State which parasite is depicted.
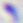
This is Toxoplasma gondii.

Summary:
  - Magnification: 400x
  - Modality: photomicrograph